Report the malaria status of this cell.
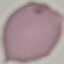

It is uninfected.

Summary:
  - Stain: Giemsa
  - Preparation: thin blood smear
  - Capture: smartphone through the microscope eyepiece
  - Image type: automatically extracted cell patch, resized to 64 × 64 pixels